Give the extent of all Plasmodium falciparum-infected red blood cells.
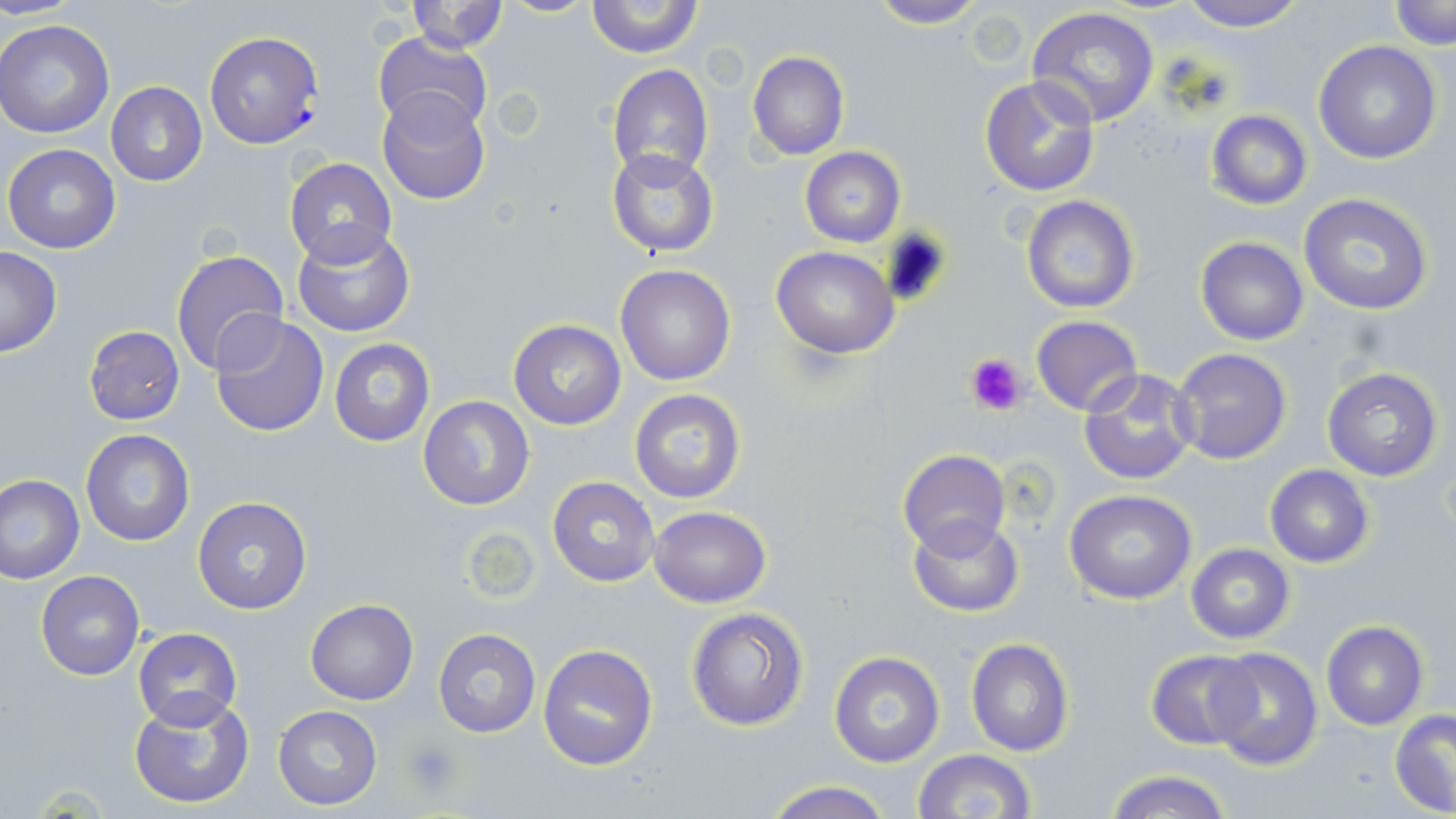

Approximate bounding boxes as (x1,y1)-(x2,y2) corner pairs in pixels.
Plasmodium falciparum-infected red blood cells: (203,31)-(325,149).

{
  "slide_level_diagnosis": "Plasmodium falciparum",
  "stain": "May-Grünwald-Giemsa",
  "field_of_view": "one of a larger specimen",
  "image_size": "1456×819 pixels",
  "preparation": "thin blood smear",
  "platelet_locations": "approximate bounding boxes as (x1,y1)-(x2,y2) corner pairs in pixels: (963,351)-(1029,418), (403,737)-(463,800)",
  "magnification": "1000x",
  "modality": "light microscopy",
  "uninfected_red_blood_cell_locations": "approximate bounding boxes as (x1,y1)-(x2,y2) corner pairs in pixels: (405,0)-(508,54), (585,0)-(702,59), (867,0)-(987,28), (1173,0)-(1311,32), (1388,1)-(1454,47), (1027,7)-(1161,127), (0,20)-(114,139), (371,33)-(493,134), (1314,41)-(1442,165), (747,51)-(848,160), (607,64)-(713,182), (979,75)-(1102,198), (105,82)-(208,186), (376,88)-(490,206), (1205,109)-(1311,210), (3,143)-(120,255), (606,147)-(720,258), (800,147)-(905,246), (283,158)-(397,266), (1299,193)-(1436,315), (1019,195)-(1140,313), (292,224)-(416,337), (1195,237)-(1309,347), (771,246)-(898,358), (0,247)-(62,357), (170,248)-(289,376), (615,264)-(737,386), (209,312)-(329,438), (1031,315)-(1142,417), (508,319)-(627,430), (82,325)-(186,425), (329,338)-(434,447), (1170,347)-(1293,465), (1322,366)-(1443,481), (1079,367)-(1201,487), (628,388)-(747,505), (418,395)-(535,511), (81,428)-(196,547), (897,449)-(1009,556), (1264,465)-(1374,568), (1,474)-(84,583), (548,477)-(660,587), (1065,490)-(1197,605), (191,496)-(313,615), (647,505)-(772,607), (907,515)-(1024,618), (1185,544)-(1295,645), (35,571)-(145,680), (304,599)-(418,704), (685,607)-(809,731), (1320,620)-(1430,732), (133,627)-(242,730), (432,628)-(541,738), (963,637)-(1075,758), (537,642)-(659,771), (1208,648)-(1324,771), (1144,649)-(1256,751), (828,651)-(945,767), (128,694)-(256,807), (273,705)-(383,811), (1390,710)-(1456,816), (913,749)-(1035,819), (1104,768)-(1235,819), (759,779)-(896,819)"
}